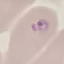

{
  "malaria_status": "parasitized",
  "preparation": "thin blood smear",
  "stain": "Giemsa",
  "capture": "smartphone camera at the microscope eyepiece",
  "image_type": "cell patch, automatically extracted from a larger field of view and resized to 64 × 64 pixels"
}